Locate every blood parasite and identify its species.
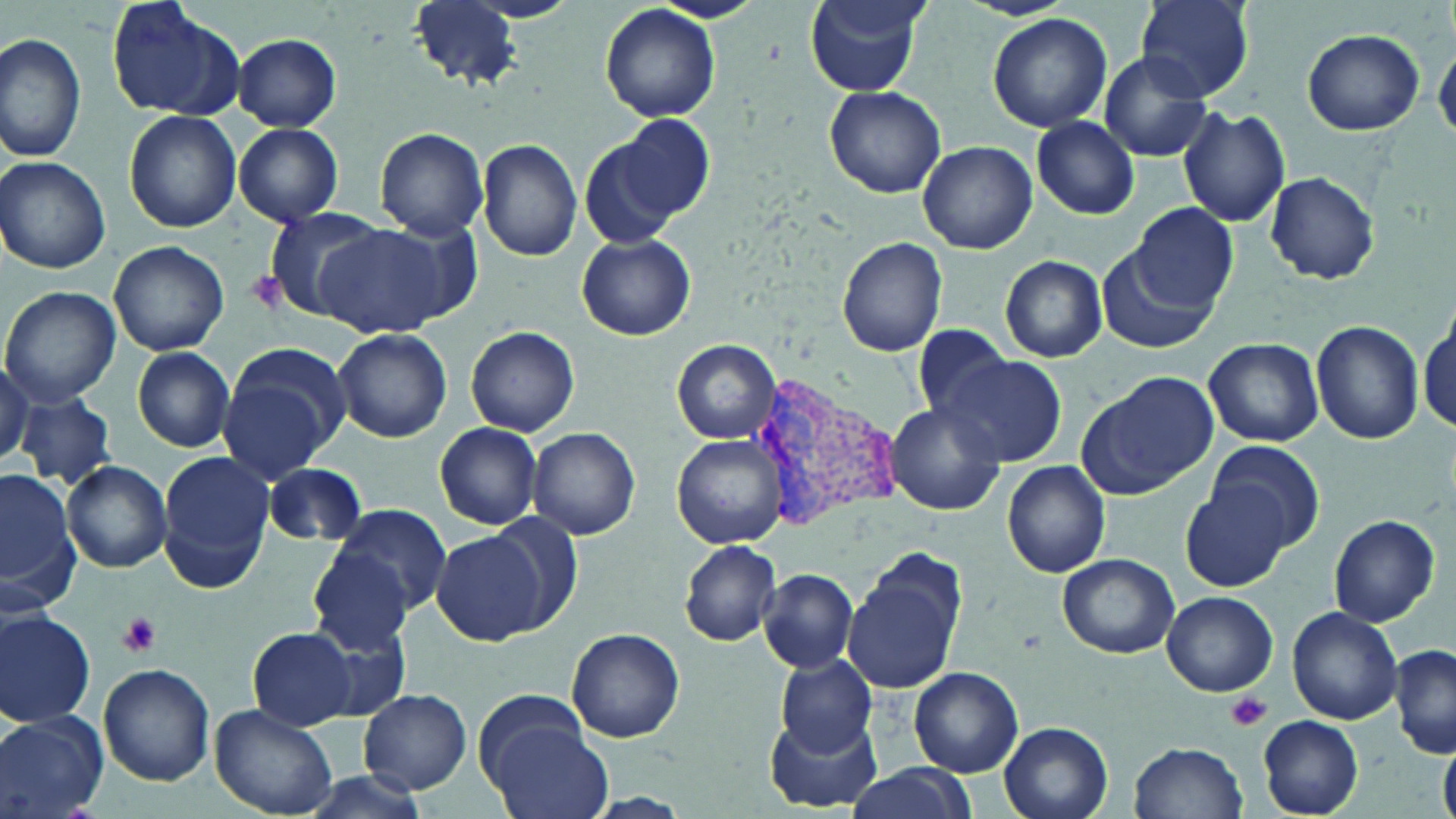
Approximate bounding boxes as named x1/y1/x2/y2 corners in pixels.
Plasmodium vivax-infected red blood cells: (x1=740, y1=364, x2=901, y2=540).
No Plasmodium falciparum, Plasmodium ovale, Plasmodium malariae, Babesia divergens, or Trypanosoma brucei observed.

Summary:
  - Platelet locations: (x1=117, y1=612, x2=162, y2=656), (x1=1227, y1=691, x2=1271, y2=731)
  - Uninfected red blood cell locations: (x1=106, y1=0, x2=242, y2=119), (x1=649, y1=0, x2=765, y2=24), (x1=804, y1=0, x2=929, y2=95), (x1=1137, y1=0, x2=1254, y2=101), (x1=410, y1=1, x2=523, y2=90), (x1=600, y1=5, x2=721, y2=123), (x1=988, y1=13, x2=1111, y2=132), (x1=1302, y1=29, x2=1424, y2=135), (x1=0, y1=31, x2=86, y2=163), (x1=231, y1=34, x2=343, y2=130), (x1=1434, y1=42, x2=1455, y2=142), (x1=1098, y1=52, x2=1212, y2=161), (x1=824, y1=86, x2=946, y2=198), (x1=1177, y1=105, x2=1291, y2=228), (x1=124, y1=110, x2=242, y2=232), (x1=604, y1=112, x2=715, y2=231), (x1=1032, y1=117, x2=1140, y2=218), (x1=235, y1=123, x2=343, y2=227), (x1=371, y1=129, x2=490, y2=239), (x1=578, y1=135, x2=683, y2=251), (x1=477, y1=138, x2=584, y2=261), (x1=918, y1=140, x2=1036, y2=254), (x1=0, y1=156, x2=111, y2=275), (x1=1263, y1=171, x2=1379, y2=284), (x1=1133, y1=204, x2=1241, y2=312), (x1=262, y1=206, x2=390, y2=316), (x1=312, y1=222, x2=461, y2=339), (x1=578, y1=234, x2=695, y2=341), (x1=837, y1=237, x2=947, y2=357), (x1=108, y1=241, x2=229, y2=357), (x1=1101, y1=244, x2=1219, y2=356), (x1=1000, y1=255, x2=1107, y2=362), (x1=1, y1=286, x2=121, y2=406), (x1=1417, y1=317, x2=1454, y2=438), (x1=1312, y1=321, x2=1425, y2=445), (x1=911, y1=323, x2=1015, y2=422), (x1=464, y1=325, x2=580, y2=437), (x1=332, y1=327, x2=453, y2=442), (x1=1203, y1=337, x2=1323, y2=447), (x1=674, y1=340, x2=779, y2=443), (x1=133, y1=347, x2=235, y2=452), (x1=216, y1=347, x2=348, y2=481), (x1=935, y1=354, x2=1066, y2=467), (x1=0, y1=359, x2=33, y2=469), (x1=1078, y1=371, x2=1217, y2=500), (x1=16, y1=394, x2=118, y2=491), (x1=885, y1=402, x2=1005, y2=515), (x1=434, y1=421, x2=543, y2=530), (x1=528, y1=426, x2=641, y2=540), (x1=673, y1=433, x2=789, y2=548), (x1=1207, y1=442, x2=1325, y2=554), (x1=157, y1=454, x2=273, y2=592), (x1=1001, y1=461, x2=1112, y2=578), (x1=60, y1=462, x2=173, y2=573), (x1=262, y1=462, x2=368, y2=547), (x1=1179, y1=467, x2=1304, y2=592), (x1=0, y1=469, x2=79, y2=616), (x1=330, y1=504, x2=452, y2=616), (x1=1329, y1=513, x2=1441, y2=627), (x1=489, y1=514, x2=586, y2=629), (x1=430, y1=528, x2=550, y2=646), (x1=677, y1=541, x2=782, y2=648), (x1=309, y1=549, x2=414, y2=656), (x1=1057, y1=553, x2=1182, y2=657), (x1=843, y1=560, x2=964, y2=695), (x1=758, y1=567, x2=860, y2=676), (x1=1162, y1=591, x2=1277, y2=695), (x1=1288, y1=606, x2=1403, y2=724), (x1=0, y1=611, x2=96, y2=728), (x1=250, y1=626, x2=360, y2=729), (x1=567, y1=628, x2=685, y2=743), (x1=1390, y1=643, x2=1456, y2=758), (x1=776, y1=654, x2=877, y2=757), (x1=97, y1=663, x2=215, y2=787), (x1=909, y1=667, x2=1023, y2=776), (x1=359, y1=689, x2=473, y2=795), (x1=473, y1=692, x2=590, y2=791), (x1=211, y1=704, x2=339, y2=818), (x1=765, y1=708, x2=881, y2=813), (x1=0, y1=711, x2=107, y2=818), (x1=1257, y1=715, x2=1363, y2=817), (x1=487, y1=722, x2=614, y2=819), (x1=999, y1=722, x2=1114, y2=819), (x1=1130, y1=741, x2=1248, y2=818), (x1=1439, y1=742, x2=1455, y2=819), (x1=842, y1=763, x2=977, y2=819)
  - Slide-level diagnosis: Plasmodium vivax
  - Magnification: 1000x
  - Preparation: thin blood film
  - Field of view: one of a larger specimen
  - Modality: optical microscopy
  - Stain: May-Grünwald-Giemsa
  - Image size: 1456×819 pixels